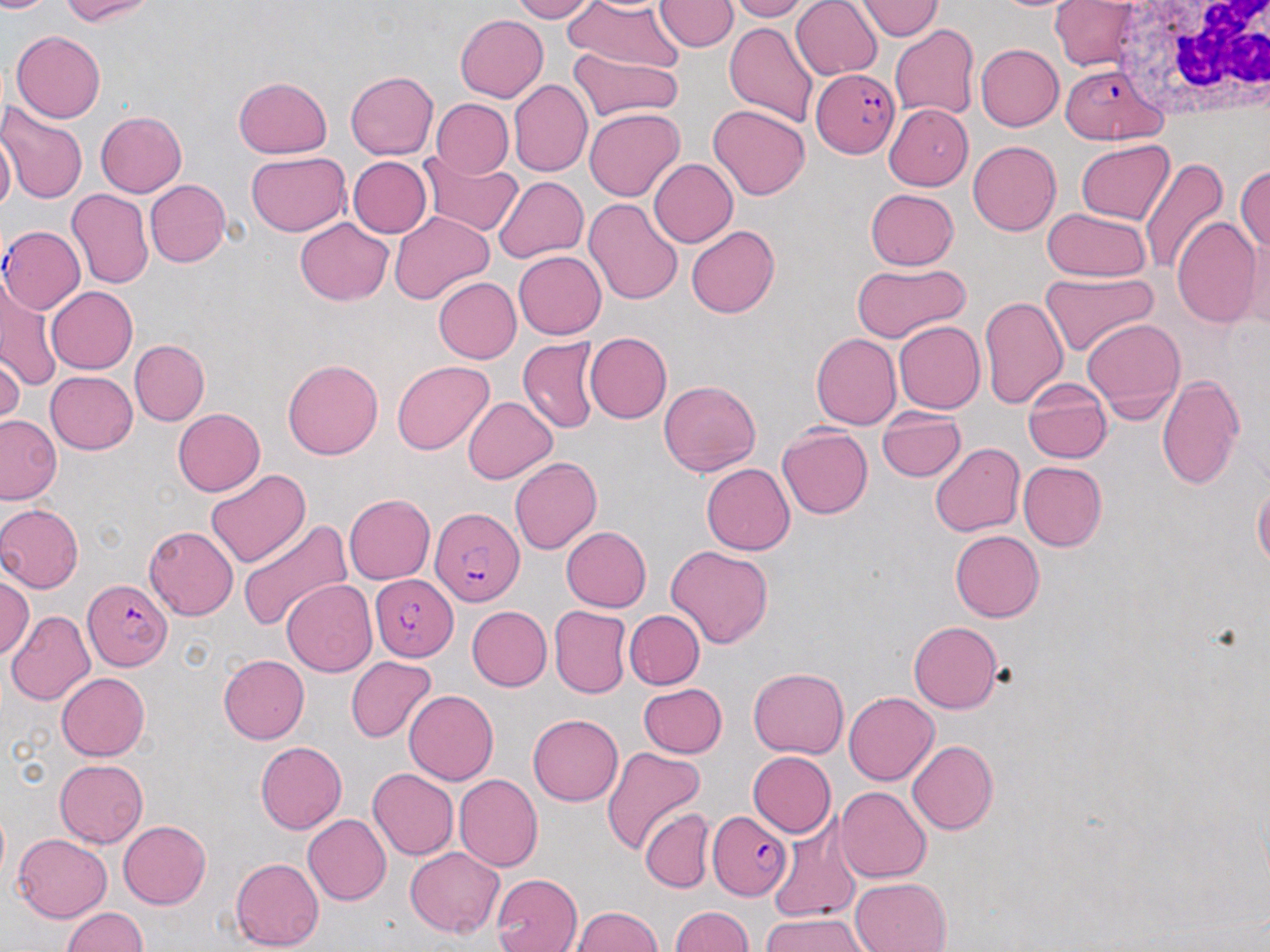
Approximate bounding boxes as (x1,y1)-(x2,y2) corner pairs in pixels. Plasmodium falciparum-infected red blood cell locations: (1058,63)-(1168,145), (812,67)-(899,159), (2,225)-(85,313), (430,507)-(524,606), (371,572)-(460,661), (83,580)-(169,672), (707,810)-(792,900). Uninfected red blood cell locations: (0,0)-(60,13), (59,0)-(157,25), (507,0)-(596,22), (565,0)-(684,71), (654,0)-(737,52), (724,0)-(809,22), (791,0)-(882,80), (855,0)-(944,41), (1049,1)-(1140,71), (455,14)-(549,102), (725,21)-(818,129), (889,24)-(979,121), (12,30)-(107,122), (976,44)-(1063,131), (569,47)-(681,122), (345,71)-(438,160), (232,76)-(333,158), (509,80)-(592,178), (432,99)-(513,178), (1,102)-(88,205), (884,103)-(973,190), (708,105)-(809,200), (583,109)-(684,201), (95,112)-(187,198), (0,129)-(15,215), (1075,140)-(1174,225), (967,141)-(1061,235), (245,151)-(350,237), (418,152)-(523,235), (347,155)-(432,238), (1138,158)-(1229,275), (649,159)-(739,248), (1236,164)-(1270,254), (494,177)-(588,262), (146,180)-(230,269), (864,187)-(959,271), (67,188)-(154,289), (582,196)-(684,306), (1042,208)-(1153,282), (388,211)-(494,304), (294,217)-(393,305), (1169,217)-(1261,329), (1239,224)-(1269,331), (686,225)-(779,318), (513,251)-(606,340), (851,262)-(970,342), (1040,272)-(1157,356), (0,277)-(61,391), (434,277)-(521,364), (45,286)-(138,374), (978,296)-(1068,409), (1083,318)-(1186,421), (894,320)-(985,415), (584,332)-(671,424), (812,334)-(901,429), (518,336)-(600,434), (130,339)-(209,425), (0,355)-(23,430), (283,359)-(383,460), (391,361)-(495,455), (45,371)-(137,454), (1156,374)-(1246,492), (1022,377)-(1113,461), (658,379)-(761,475), (463,397)-(558,484), (172,408)-(265,496), (878,408)-(966,482), (0,414)-(61,505), (776,426)-(872,519), (930,442)-(1025,536), (510,458)-(602,554), (1018,462)-(1107,551), (701,463)-(795,554), (205,469)-(311,569), (1252,484)-(1270,569), (343,493)-(435,584), (0,503)-(85,593), (237,518)-(352,633), (143,525)-(238,620), (561,525)-(652,611), (950,529)-(1044,622), (666,545)-(774,648), (0,575)-(34,660), (281,579)-(377,677), (549,605)-(632,699), (467,606)-(552,690), (7,610)-(96,706), (624,610)-(704,689), (908,620)-(1002,713), (218,654)-(309,743), (346,656)-(436,742), (749,667)-(847,758), (57,672)-(149,760), (637,684)-(727,758), (403,689)-(498,785), (844,692)-(938,785), (527,714)-(623,806), (256,741)-(347,834), (908,741)-(999,835), (601,746)-(707,854), (748,751)-(836,837), (54,758)-(148,848), (368,769)-(459,860), (454,773)-(543,872), (835,786)-(931,882), (639,807)-(714,893), (303,814)-(391,906), (767,817)-(862,924), (117,820)-(210,909), (11,833)-(111,922), (405,848)-(504,938), (231,856)-(324,952), (491,873)-(582,952), (850,877)-(951,952), (567,906)-(663,951), (668,906)-(752,952), (61,907)-(146,952), (761,912)-(871,952). White blood cell locations: (1111,0)-(1270,118). Slide-level diagnosis: Plasmodium falciparum. Light microscopy. May-Grünwald-Giemsa stain. Thin blood smear. Image is 1270×952 pixels. Captured at 1000x magnification. One field of a larger specimen.